Name the cell type shown.
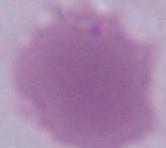

An erythrocyte.

Summary:
  - Modality: micrograph
  - Magnification: 1000x